Name the parasite shown.
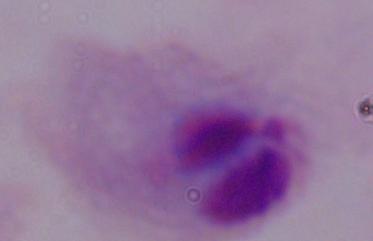

This is a trichomonad.

Summary:
  - Magnification: 1000x
  - Modality: micrograph